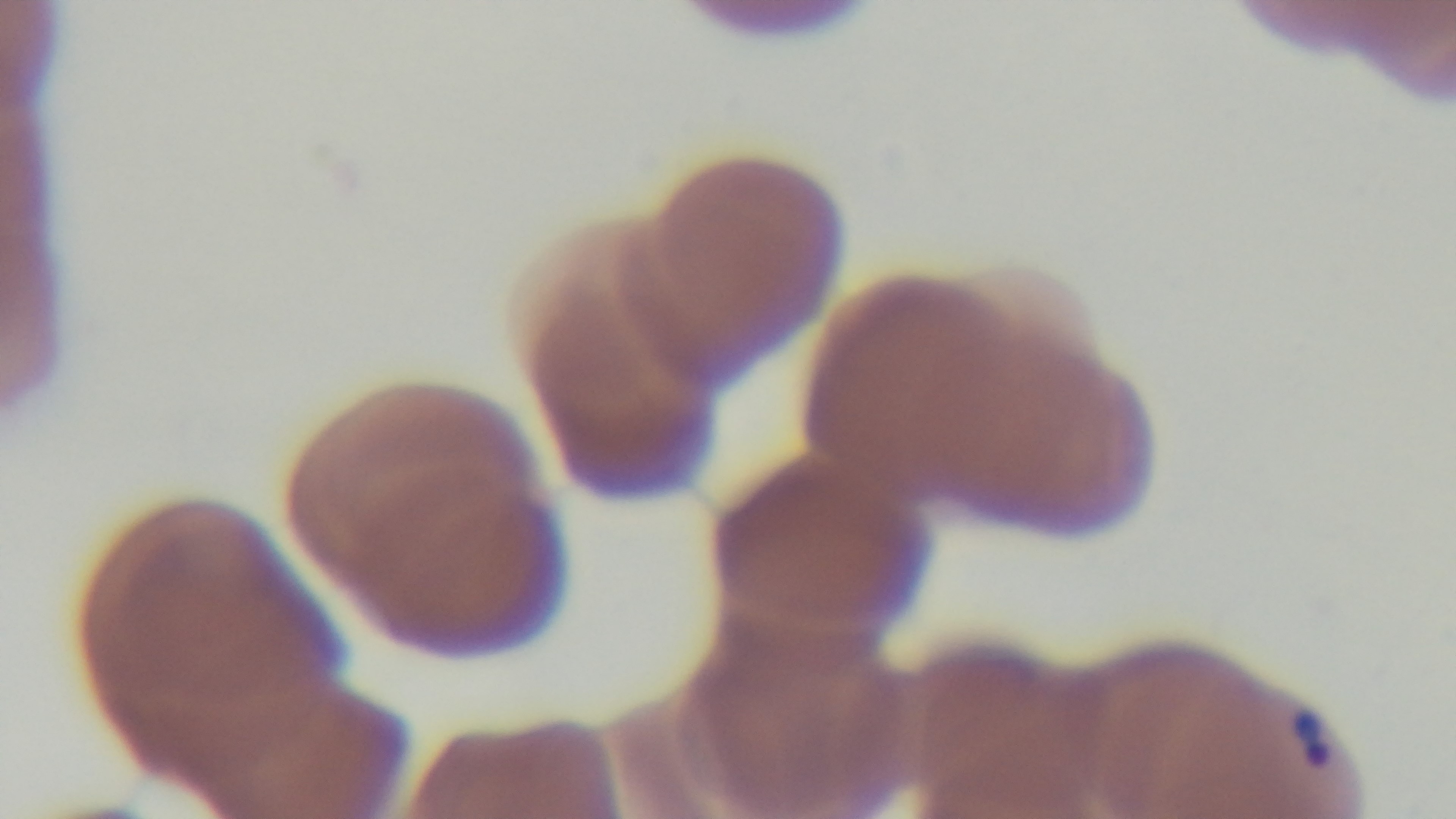
Light microscopy. Malaria status: infected. One field from the slide. Giemsa stain. Preparation: thin smear. Mounted 4K digital camera. Oil-immersion objective, 100x.